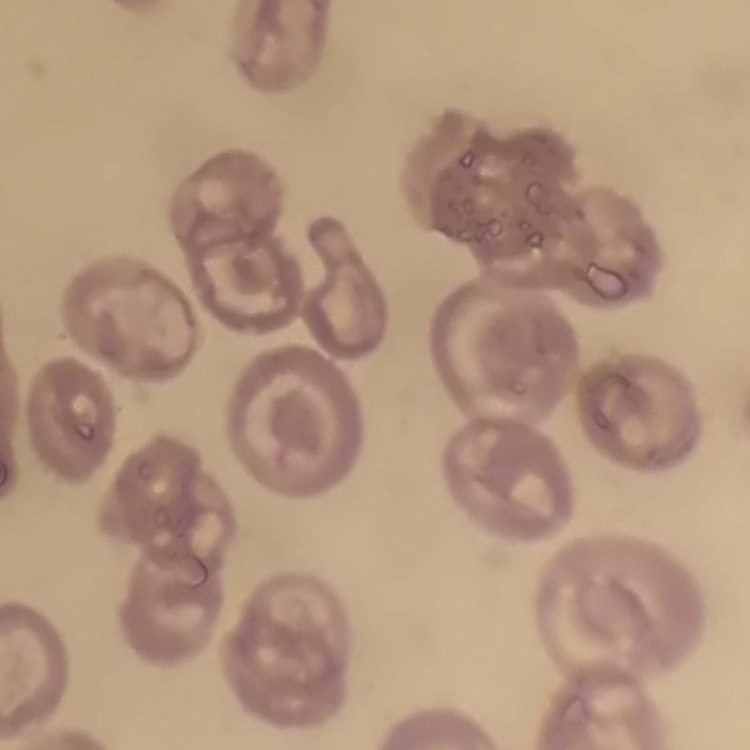

red_blood_cell_morphology: no rouleaux formation
image_type: square crop of a larger photomicrograph
stain: Field's or Giemsa
preparation: thin blood smear